Give the preparation type.
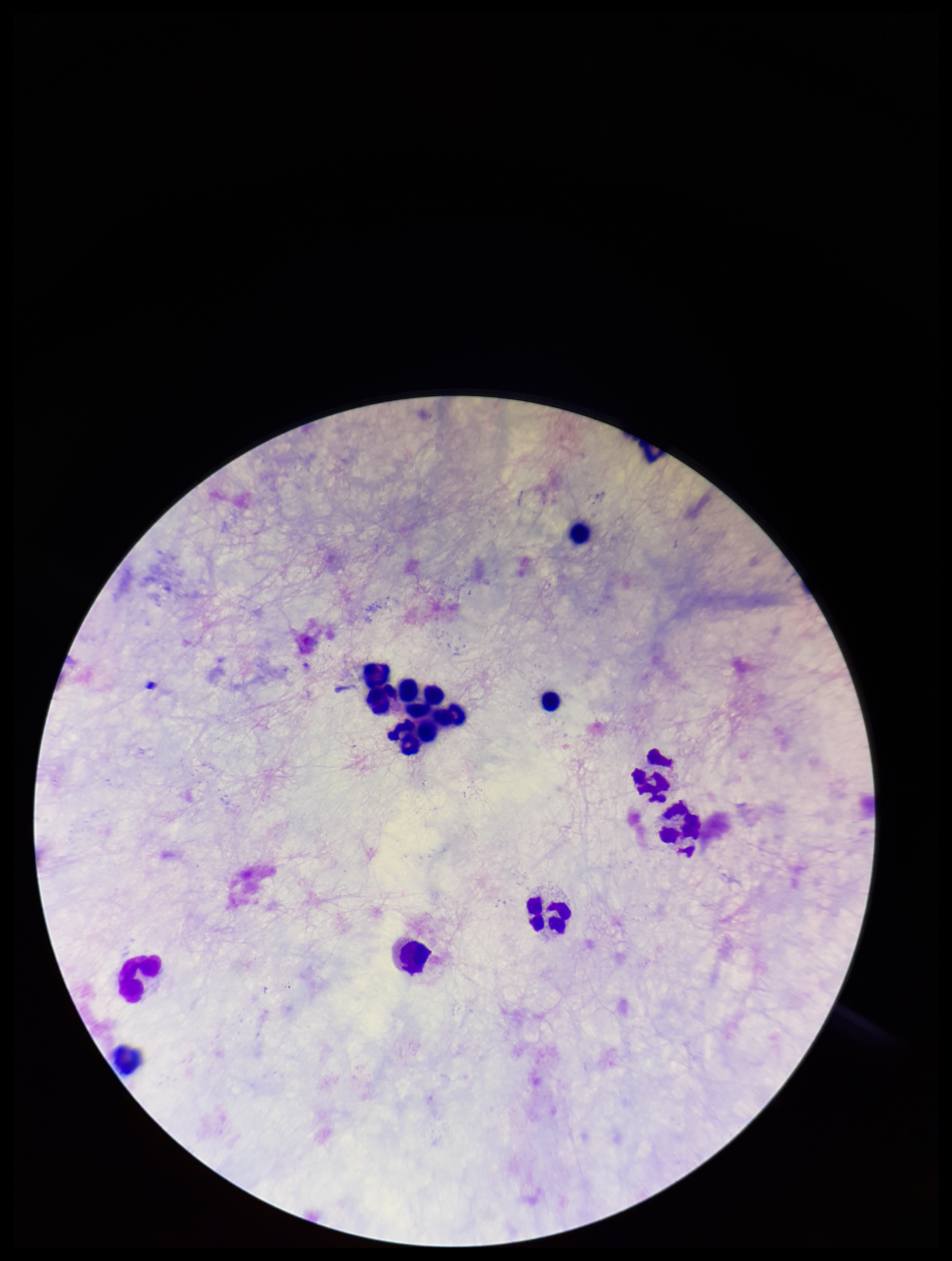
A thick smear.

Leukocyte count: 15. Image is 952×1261 pixels. Patient malaria status: negative. Parasite count: 0. Giemsa stain. Smartphone photograph taken through the eyepiece of a microscope. Plasmodium parasites: none seen. One field from this slide.